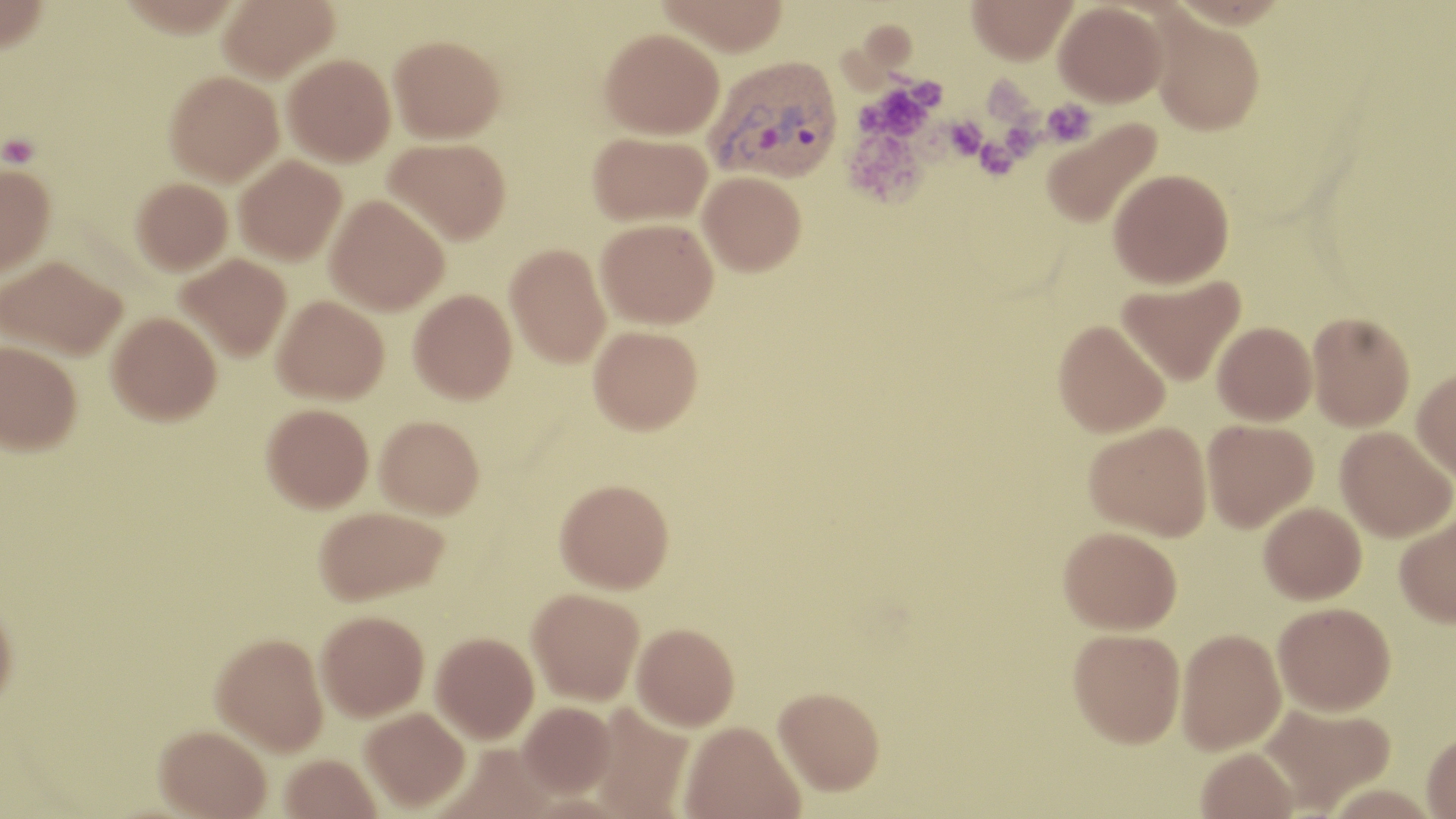
slide-level diagnosis = Plasmodium vivax
stain = May-Grünwald-Giemsa
magnification = 1000x
uninfected red blood cell locations = approximate bounding boxes as (x1,y1)-(x2,y2) corner pairs in pixels: (0,0)-(49,53), (218,0)-(339,83), (656,0)-(789,56), (966,0)-(1077,65), (1054,2)-(1168,106), (1150,13)-(1265,135), (599,27)-(724,139), (388,35)-(504,143), (282,54)-(395,166), (164,71)-(283,185), (1041,118)-(1163,229), (587,131)-(712,226), (384,137)-(511,244), (234,155)-(346,265), (0,164)-(55,276), (1109,168)-(1234,288), (698,171)-(806,275), (131,177)-(233,275), (326,195)-(449,315), (596,217)-(719,328), (505,243)-(610,368), (175,254)-(292,361), (1,256)-(127,360), (1117,275)-(1246,386), (409,289)-(516,403), (272,295)-(389,403), (107,311)-(222,425), (1307,311)-(1415,431), (1053,320)-(1170,438), (1212,322)-(1317,425), (589,325)-(703,435), (1,340)-(82,456), (1411,368)-(1456,481), (261,403)-(372,514), (375,416)-(485,521), (1202,419)-(1317,532), (1084,421)-(1212,540), (1336,426)-(1455,542), (554,480)-(674,595), (1259,502)-(1367,604), (314,508)-(448,607), (1395,511)-(1456,628), (1058,526)-(1182,634), (527,589)-(644,705), (0,602)-(18,716), (1273,602)-(1396,715), (315,611)-(429,721), (632,623)-(740,731), (1067,628)-(1186,748), (1176,628)-(1286,754), (211,633)-(328,755), (431,633)-(538,743), (773,685)-(885,795), (519,701)-(616,798), (1259,702)-(1396,812), (588,703)-(693,818), (360,707)-(470,811), (680,721)-(804,819), (153,725)-(272,818), (1422,729)-(1456,818), (1196,747)-(1299,819), (278,754)-(382,818)
platelet locations = approximate bounding boxes as (x1,y1)-(x2,y2) corner pairs in pixels: (981,76)-(1039,126), (855,79)-(941,144), (1040,99)-(1096,147), (1005,114)-(1051,161), (939,115)-(988,164), (843,127)-(930,209), (1,133)-(40,168), (972,133)-(1025,182)
Plasmodium vivax-infected red blood cell locations = approximate bounding boxes as (x1,y1)-(x2,y2) corner pairs in pixels: (705,55)-(843,182)
field of view = one of a larger specimen
image size = 1456×819 pixels
preparation = thin blood smear
modality = optical microscopy